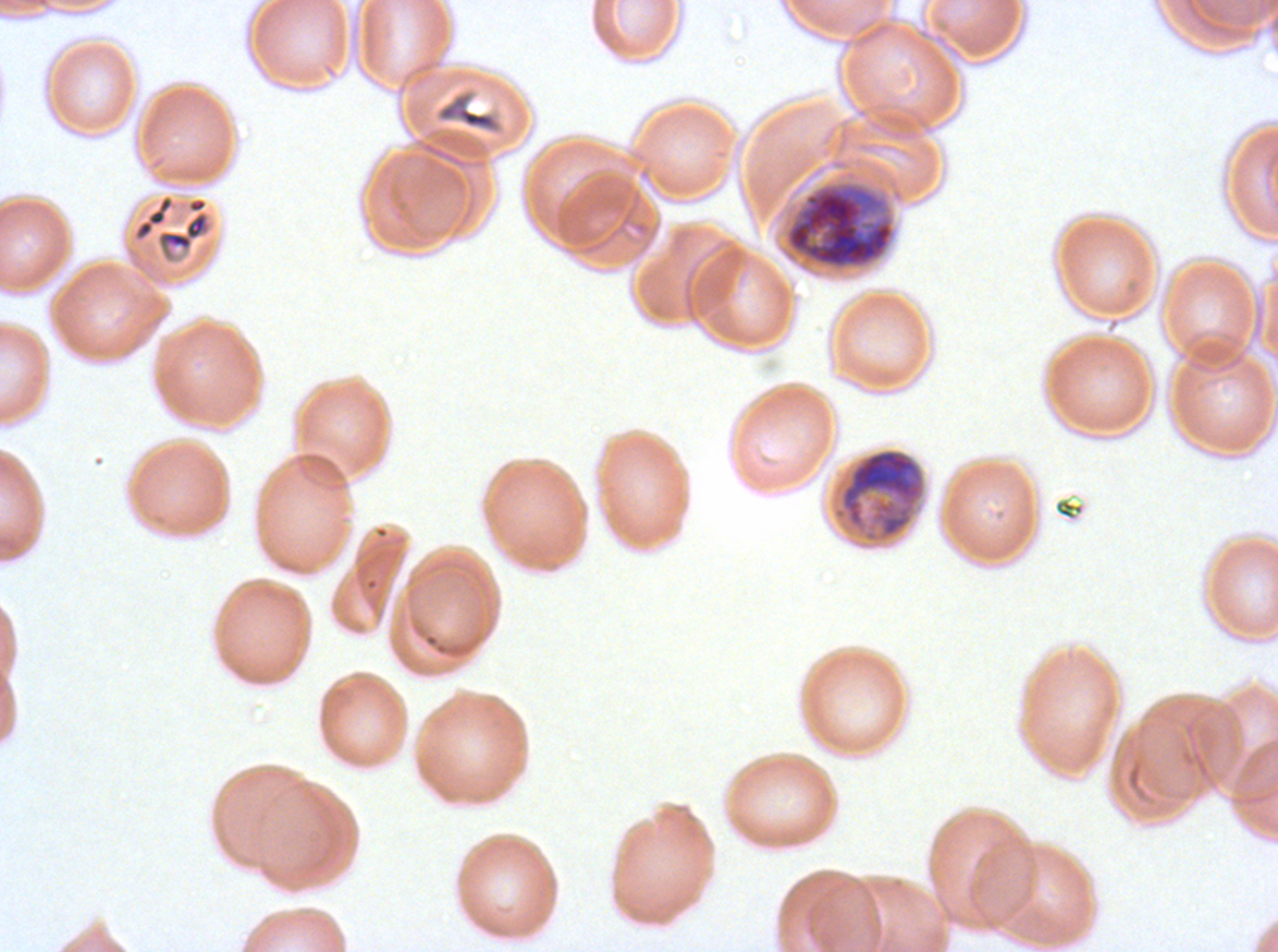
Approximate bounding rectangles given as corner coordinates in pixels from the top-left.
Summary:
  - Early schizont locations: (x1=783, y1=179, x2=896, y2=272), (x1=830, y1=446, x2=928, y2=545)
  - Debris locations: (x1=435, y1=88, x2=504, y2=135), (x1=154, y1=195, x2=213, y2=263)
  - Field of view: one sub-image of a larger composite
  - Preparation: thin blood smear
  - Stain: Giemsa
  - Specimen: Plasmodium falciparum from a patient in The Gambia, cultured ex vivo for 24 to 48 hours
  - Image size: 1278×952 pixels